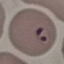
Result: malaria parasites detected. Thin blood film. Automatically extracted cell patch, resized to 64 × 64 pixels. Photographed with a smartphone camera at the microscope eyepiece. Giemsa stain.